Name the parasite shown.
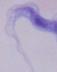

A trypanosome.

Captured at 1000x magnification. Micrograph.